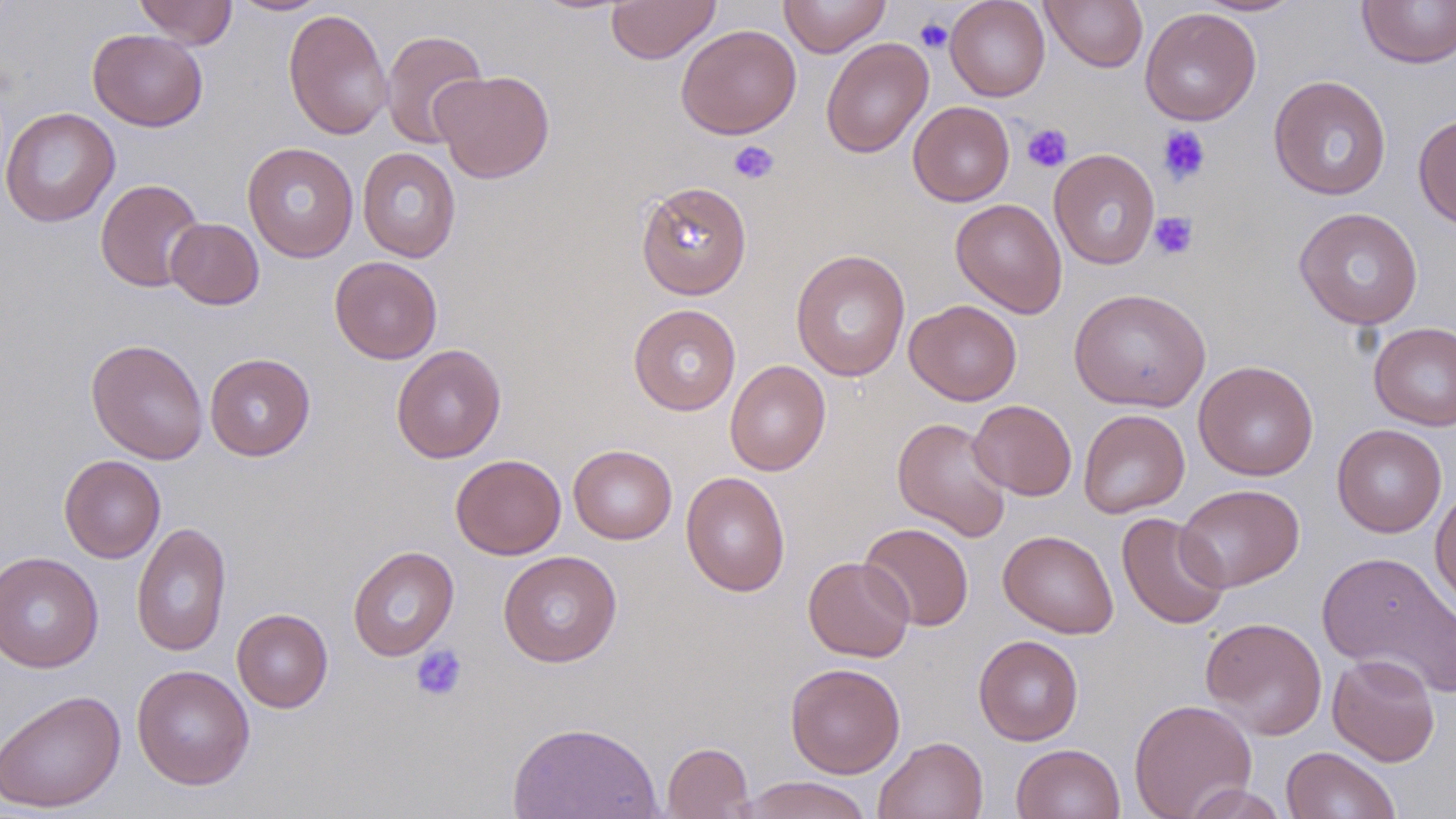

Summary:
  - Coordinate format: approximate bounding boxes as (x1, y1, x2, y2) in pixels
  - Uninfected red blood cell locations: (134, 0, 237, 49), (607, 0, 720, 64), (778, 0, 891, 57), (945, 0, 1050, 101), (1041, 0, 1148, 72), (1191, 0, 1307, 17), (1357, 0, 1456, 68), (226, 1, 335, 16), (1139, 7, 1261, 126), (284, 8, 393, 140), (676, 24, 801, 140), (88, 28, 208, 131), (380, 29, 488, 150), (821, 37, 933, 158), (431, 69, 555, 184), (1268, 75, 1391, 201), (908, 101, 1015, 206), (0, 106, 120, 227), (1413, 113, 1456, 230), (243, 141, 358, 262), (357, 147, 461, 262), (1048, 149, 1160, 270), (95, 178, 205, 293), (636, 180, 752, 299), (951, 198, 1067, 318), (1294, 207, 1423, 330), (165, 218, 264, 310), (791, 249, 911, 382), (329, 256, 443, 364), (1068, 287, 1211, 413), (904, 299, 1022, 405), (628, 304, 741, 416), (1369, 322, 1456, 431), (85, 338, 209, 464), (391, 343, 506, 463), (204, 353, 315, 460), (725, 359, 830, 476), (1193, 360, 1319, 480), (968, 399, 1077, 501), (1078, 409, 1190, 518), (893, 417, 1013, 541), (1332, 424, 1447, 537), (568, 444, 677, 544), (58, 454, 166, 563), (450, 454, 566, 559), (680, 471, 791, 597), (1175, 484, 1304, 592), (1430, 484, 1456, 613), (1117, 512, 1230, 630), (131, 522, 232, 657), (859, 522, 974, 631), (998, 529, 1119, 638), (348, 545, 459, 660), (498, 550, 622, 667), (1317, 550, 1456, 697), (0, 551, 103, 673), (803, 556, 914, 662), (232, 608, 333, 713), (1200, 616, 1328, 740), (973, 635, 1084, 745), (1327, 653, 1440, 766), (785, 662, 905, 778), (131, 664, 255, 790), (0, 688, 126, 813), (1128, 698, 1257, 819), (507, 719, 663, 819), (873, 735, 989, 819), (662, 741, 754, 818), (1011, 743, 1125, 819), (1281, 746, 1400, 819), (734, 776, 875, 819), (1183, 783, 1290, 818)
  - Platelet locations: (914, 17, 953, 53), (1022, 124, 1072, 173), (1157, 126, 1211, 185), (728, 140, 779, 184), (1149, 212, 1199, 260), (410, 644, 468, 702)
  - Slide-level diagnosis: negative for blood parasites
  - Field of view: single
  - Modality: light microscopy
  - Stain: May-Grünwald-Giemsa
  - Preparation: thin blood smear
  - Magnification: 1000x
  - Image size: 1456×819 pixels